Name the parasite shown.
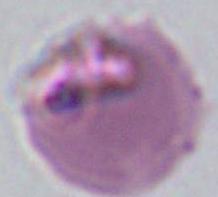

Plasmodium.

Micrograph. 400x or 1000x magnification.